Identify the parasite.
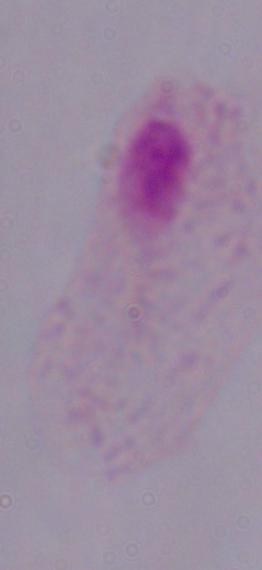

A trichomonad.

Summary:
  - Magnification: 1000x
  - Modality: photomicrograph